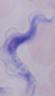
identification: trypanosome
modality: micrograph
magnification: 1000x